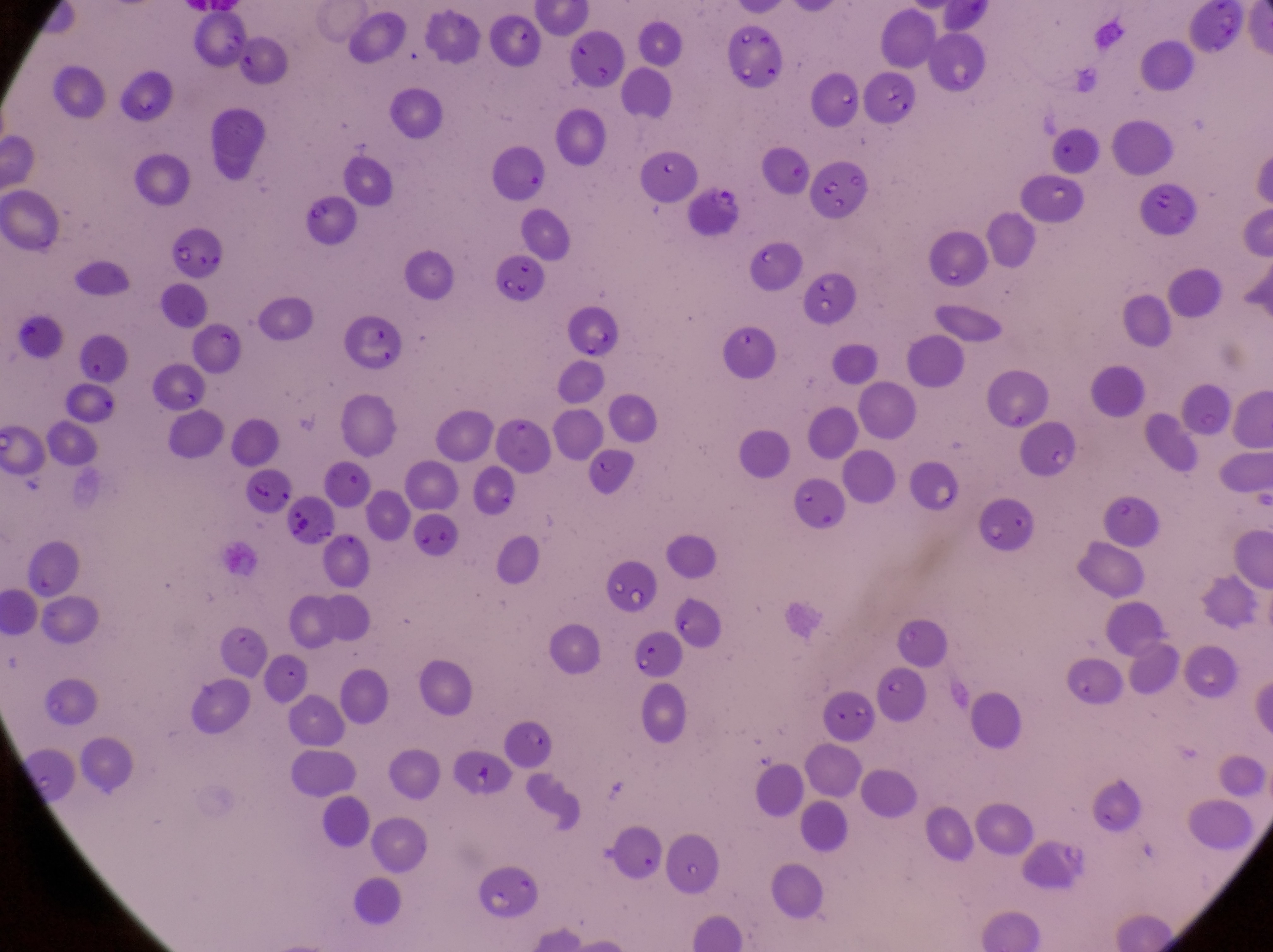

Approximate bounding boxes as {left, top, right, bottom} in pixels. Parasitised red blood cell locations: {686, 185, 746, 237}, {169, 222, 224, 280}, {245, 469, 300, 517}. Image is 1273×952 pixels. Thin blood smear. One field of view. Magnification of 1000x. Photographed through the eyepiece of an Olympus CX-23 microscope with a smartphone camera. Sample from Uganda.